Classify this cell by malaria status.
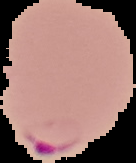
It is parasitized.

Summary:
  - Image size: 136×163 pixels
  - Image type: cell region segmented out of the field of view; surrounding area masked to black
  - Preparation: thin blood smear